Point out each malaria parasite.
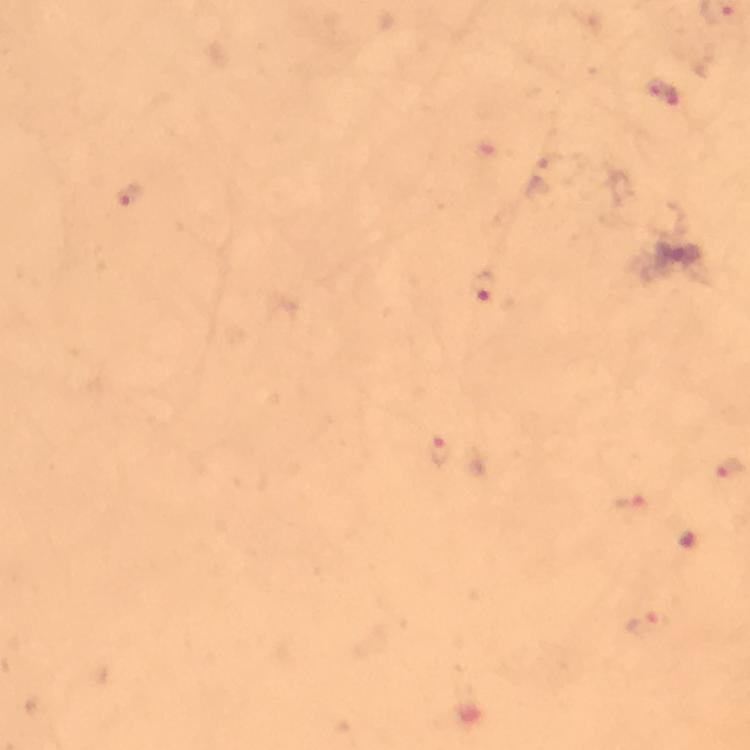
Approximate centers as (x, y) in pixels.
Malaria parasites: (662, 91), (128, 198), (485, 290), (438, 450), (629, 506), (647, 626).

Summary:
  - Capture: smartphone mounted on the microscope
  - Context: from a diagnostic examination for malaria
  - Preparation: thick blood film
  - Stain: Giemsa
  - Immersion oil: applied
  - Magnification: 100x
  - Image size: 750×750 pixels
  - Cropped from: one field of view